Give the position of every Plasmodium parasite.
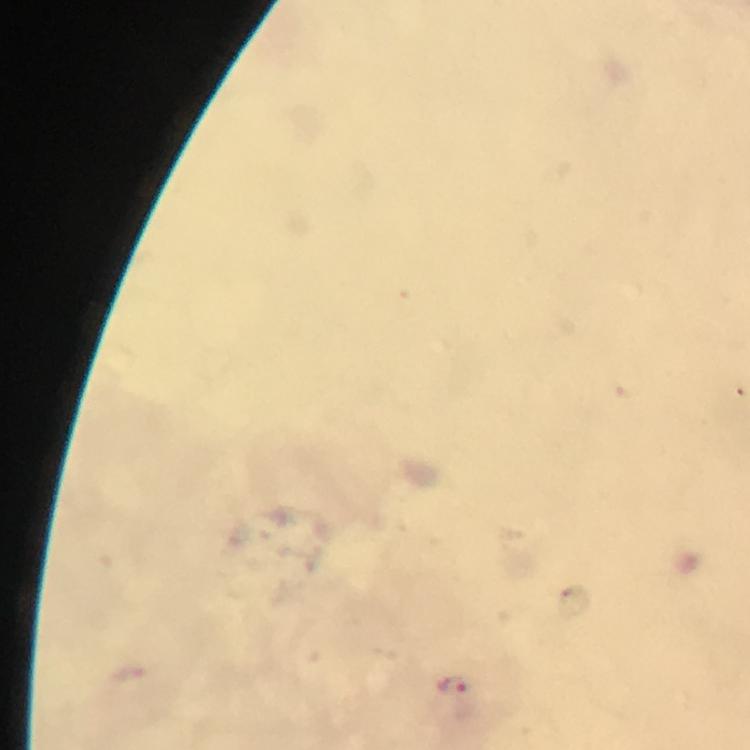
Approximate centers as (x, y) in pixels.
Plasmodium parasites: (453, 687).

Immersion oil was used. From a malaria diagnostic workup. A crop from one field of view. Smartphone photograph taken through a microscope. At 100x magnification. Giemsa stain. Image is 750×750 pixels. Thick blood smear.